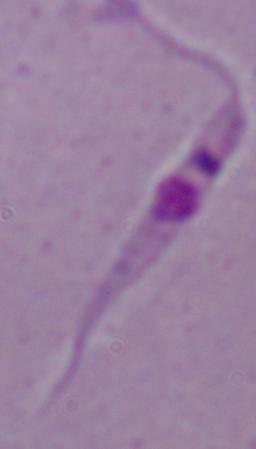

modality = micrograph
identification = Leishmania
magnification = 1000x